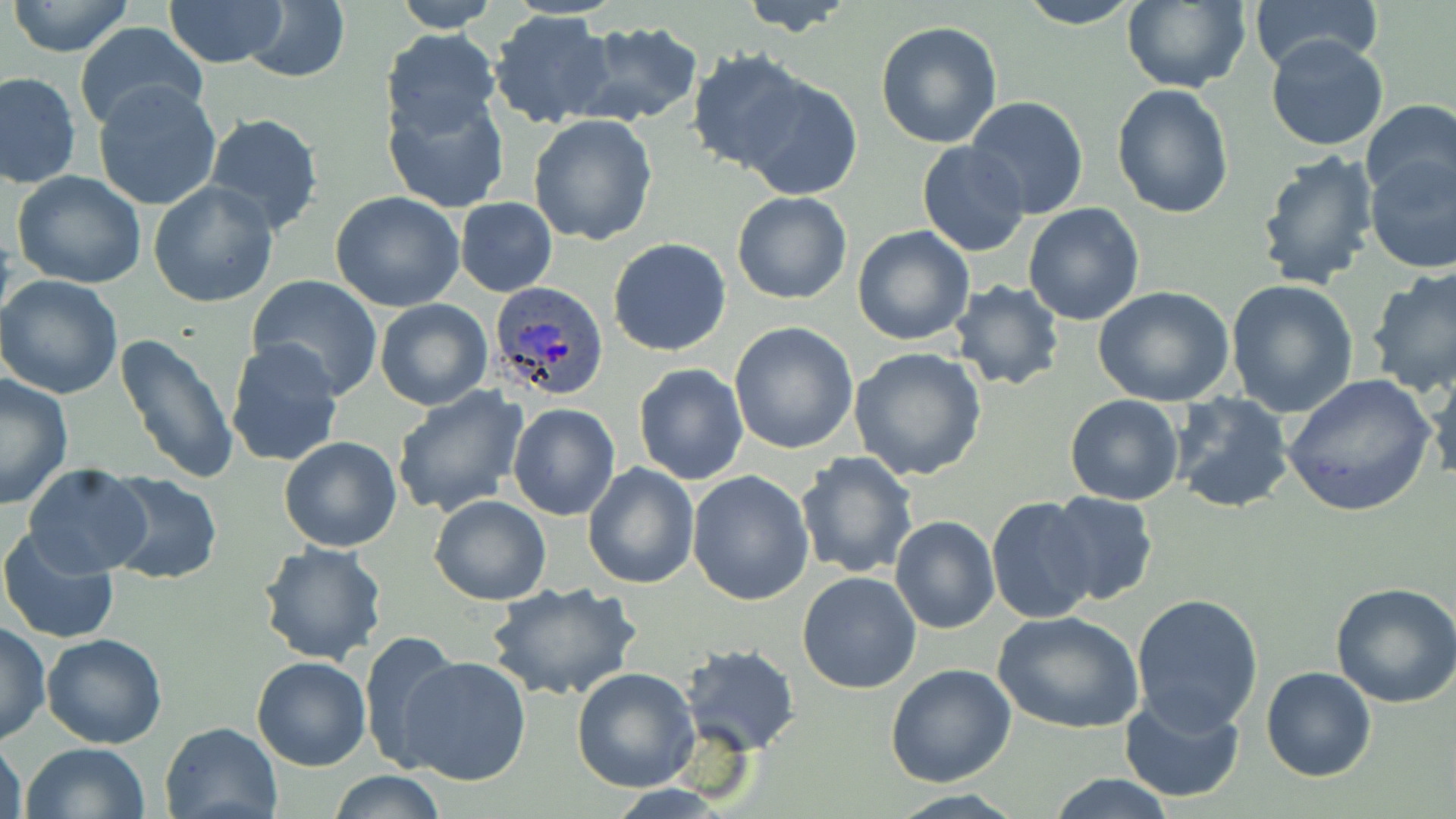

Approximate bounding boxes as named x1/y1/x2/y2 corners in pixels. Plasmodium ovale-infected red blood cell locations: (x1=489, y1=281, x2=612, y2=402). Uninfected red blood cell locations: (x1=163, y1=0, x2=289, y2=70), (x1=389, y1=0, x2=499, y2=32), (x1=738, y1=0, x2=860, y2=36), (x1=1014, y1=0, x2=1145, y2=28), (x1=1248, y1=0, x2=1383, y2=73), (x1=8, y1=1, x2=134, y2=56), (x1=243, y1=1, x2=349, y2=83), (x1=1119, y1=2, x2=1251, y2=92), (x1=488, y1=10, x2=615, y2=130), (x1=572, y1=20, x2=705, y2=128), (x1=875, y1=21, x2=1003, y2=149), (x1=72, y1=22, x2=208, y2=135), (x1=381, y1=27, x2=501, y2=136), (x1=1264, y1=34, x2=1390, y2=152), (x1=684, y1=50, x2=814, y2=174), (x1=1, y1=72, x2=79, y2=189), (x1=739, y1=75, x2=862, y2=198), (x1=93, y1=81, x2=221, y2=211), (x1=1111, y1=83, x2=1235, y2=218), (x1=383, y1=90, x2=509, y2=214), (x1=966, y1=96, x2=1091, y2=220), (x1=1359, y1=100, x2=1456, y2=204), (x1=200, y1=112, x2=326, y2=237), (x1=527, y1=114, x2=658, y2=247), (x1=917, y1=141, x2=1029, y2=256), (x1=1256, y1=148, x2=1383, y2=292), (x1=1363, y1=156, x2=1456, y2=272), (x1=10, y1=170, x2=149, y2=292), (x1=149, y1=180, x2=278, y2=306), (x1=330, y1=191, x2=466, y2=312), (x1=732, y1=191, x2=853, y2=305), (x1=456, y1=198, x2=557, y2=295), (x1=1023, y1=202, x2=1145, y2=326), (x1=852, y1=225, x2=975, y2=346), (x1=608, y1=238, x2=731, y2=356), (x1=1367, y1=266, x2=1456, y2=397), (x1=0, y1=274, x2=124, y2=400), (x1=246, y1=274, x2=384, y2=397), (x1=1226, y1=278, x2=1359, y2=415), (x1=950, y1=280, x2=1065, y2=391), (x1=1094, y1=286, x2=1237, y2=406), (x1=373, y1=298, x2=493, y2=410), (x1=729, y1=321, x2=859, y2=453), (x1=113, y1=332, x2=241, y2=485), (x1=224, y1=338, x2=346, y2=470), (x1=848, y1=347, x2=989, y2=482), (x1=1424, y1=357, x2=1456, y2=485), (x1=632, y1=363, x2=748, y2=485), (x1=0, y1=372, x2=76, y2=509), (x1=1282, y1=373, x2=1436, y2=518), (x1=390, y1=386, x2=528, y2=518), (x1=1170, y1=393, x2=1294, y2=514), (x1=1064, y1=394, x2=1185, y2=506), (x1=507, y1=401, x2=621, y2=522), (x1=278, y1=436, x2=402, y2=552), (x1=794, y1=453, x2=917, y2=579), (x1=583, y1=462, x2=700, y2=589), (x1=23, y1=464, x2=152, y2=577), (x1=687, y1=471, x2=815, y2=607), (x1=102, y1=472, x2=223, y2=585), (x1=1046, y1=491, x2=1158, y2=606), (x1=429, y1=494, x2=552, y2=606), (x1=987, y1=497, x2=1098, y2=624), (x1=890, y1=515, x2=1000, y2=634), (x1=1, y1=526, x2=120, y2=646), (x1=255, y1=542, x2=389, y2=666), (x1=797, y1=570, x2=923, y2=694), (x1=486, y1=580, x2=643, y2=703), (x1=1331, y1=580, x2=1456, y2=708), (x1=1131, y1=593, x2=1263, y2=734), (x1=993, y1=611, x2=1143, y2=734), (x1=0, y1=621, x2=51, y2=747), (x1=357, y1=632, x2=460, y2=773), (x1=41, y1=634, x2=166, y2=749), (x1=679, y1=643, x2=800, y2=754), (x1=251, y1=656, x2=373, y2=771), (x1=398, y1=657, x2=531, y2=786), (x1=886, y1=664, x2=1016, y2=788), (x1=572, y1=667, x2=700, y2=792), (x1=1262, y1=667, x2=1376, y2=782), (x1=1119, y1=693, x2=1247, y2=804), (x1=160, y1=720, x2=284, y2=819), (x1=0, y1=735, x2=26, y2=819), (x1=21, y1=742, x2=150, y2=819), (x1=326, y1=771, x2=449, y2=818), (x1=1045, y1=773, x2=1179, y2=818), (x1=882, y1=790, x2=1029, y2=819). Slide-level diagnosis: Plasmodium ovale. One field of a larger specimen. Thin blood film. Light microscopy. May-Grünwald-Giemsa-stained preparation. Image is 1456×819 pixels. Captured at 1000x magnification.